Outline each Plasmodium falciparum-infected red blood cell.
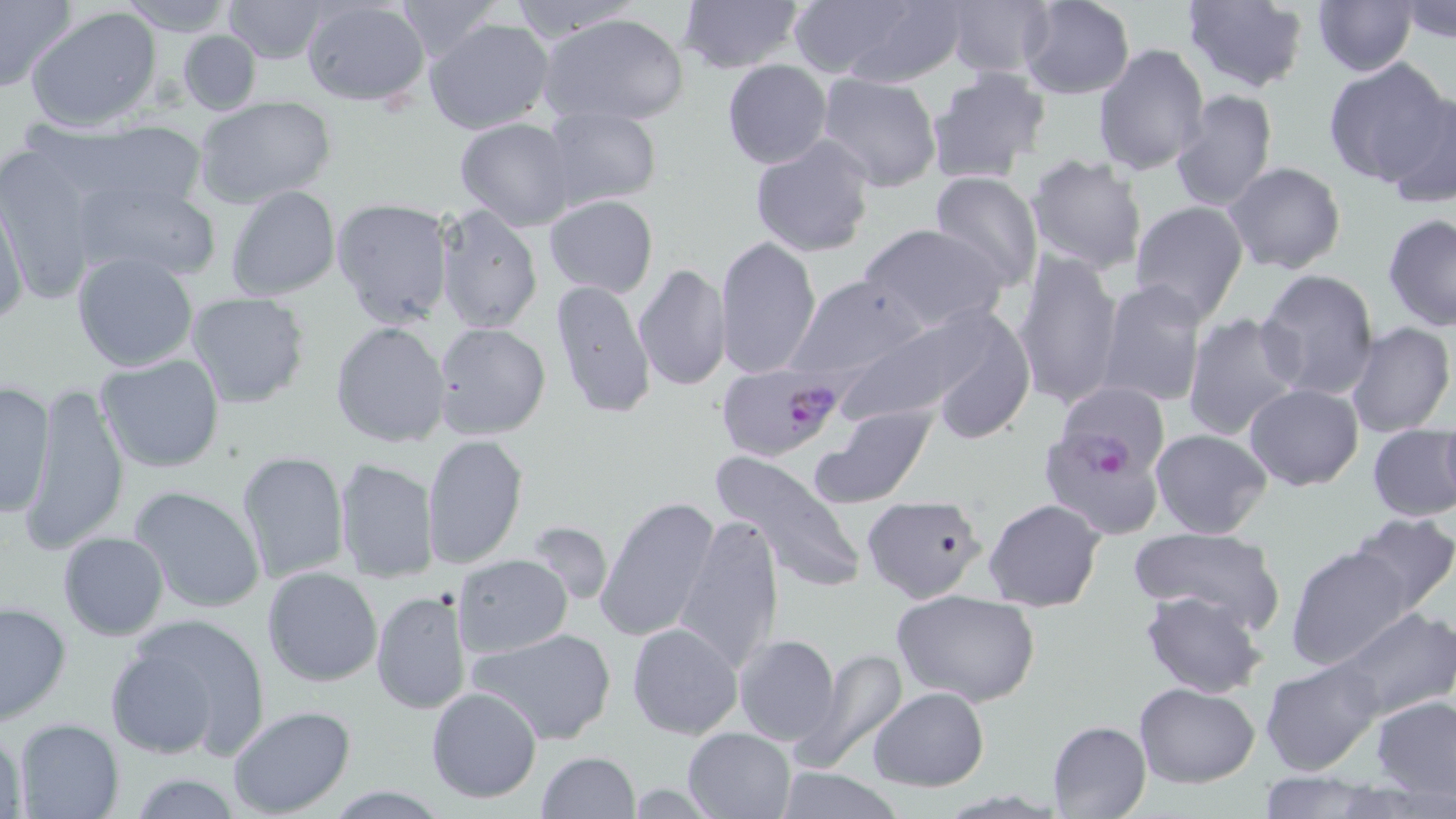

Approximate bounding boxes as (x1, y1, x2, y2) in pixels.
Plasmodium falciparum-infected red blood cells: (716, 364, 839, 462), (1039, 424, 1165, 539).

{
  "slide_level_diagnosis": "Plasmodium falciparum",
  "image_size": "1456×819 pixels",
  "field_of_view": "one of a larger specimen",
  "preparation": "thin blood film",
  "modality": "optical microscopy",
  "uninfected_red_blood_cell_locations": "approximate bounding boxes as (x1, y1, x2, y2) in pixels: (0, 0, 77, 98), (119, 0, 236, 32), (220, 0, 332, 63), (392, 0, 505, 64), (504, 0, 638, 47), (677, 0, 804, 75), (941, 0, 1057, 80), (1016, 0, 1135, 100), (1179, 0, 1310, 93), (1311, 0, 1418, 77), (1398, 0, 1456, 44), (300, 1, 432, 108), (784, 1, 966, 86), (25, 6, 163, 130), (538, 11, 690, 127), (424, 17, 557, 136), (177, 31, 262, 115), (1093, 42, 1211, 176), (1325, 58, 1454, 187), (722, 59, 832, 169), (927, 68, 1055, 186), (816, 72, 944, 194), (1169, 89, 1279, 213), (1382, 91, 1456, 206), (192, 94, 339, 208), (539, 105, 661, 211), (454, 117, 577, 231), (69, 123, 213, 227), (748, 133, 877, 259), (0, 146, 104, 306), (1024, 154, 1149, 274), (1223, 160, 1348, 274), (928, 170, 1045, 292), (73, 171, 221, 285), (226, 185, 342, 300), (1, 193, 30, 328), (544, 194, 658, 298), (330, 198, 454, 330), (1129, 200, 1249, 323), (435, 205, 543, 333), (1382, 213, 1456, 332), (859, 222, 1007, 333), (715, 234, 821, 380), (1011, 248, 1122, 410), (71, 251, 198, 373), (631, 263, 732, 393), (1255, 267, 1382, 399), (790, 274, 926, 383), (1098, 278, 1209, 408), (550, 280, 658, 419), (186, 290, 310, 408), (909, 302, 1035, 445), (1180, 312, 1305, 443), (331, 321, 450, 449), (432, 321, 551, 439), (825, 321, 977, 430), (1343, 322, 1453, 438), (95, 352, 226, 473), (0, 381, 55, 521), (17, 382, 132, 553), (1244, 383, 1363, 491), (815, 405, 937, 507), (1438, 413, 1456, 515), (1367, 424, 1455, 522), (1149, 429, 1273, 540), (421, 433, 529, 570), (712, 450, 866, 592), (235, 451, 349, 584), (335, 457, 437, 584), (129, 485, 268, 616), (595, 493, 721, 642), (862, 495, 987, 603), (983, 498, 1105, 612), (678, 512, 787, 669), (1348, 513, 1456, 616), (523, 521, 613, 608), (1131, 525, 1284, 638), (58, 531, 169, 642), (1284, 542, 1416, 672), (451, 554, 573, 658), (261, 565, 383, 686), (891, 588, 1043, 708), (371, 589, 472, 715), (1140, 589, 1267, 697), (0, 598, 73, 725), (1333, 607, 1455, 719), (109, 617, 268, 761), (627, 621, 743, 738), (470, 625, 618, 746), (733, 634, 841, 746), (795, 648, 908, 771), (1260, 658, 1383, 775), (1134, 682, 1260, 786), (425, 685, 542, 803), (868, 686, 989, 791), (1371, 694, 1456, 799), (226, 705, 356, 818), (2, 715, 29, 818), (11, 717, 124, 819), (1048, 719, 1152, 819), (682, 726, 798, 818), (536, 752, 641, 819), (774, 765, 902, 819), (1254, 771, 1391, 818), (124, 773, 247, 817), (322, 785, 452, 817)",
  "magnification": "1000x",
  "stain": "May-Grünwald-Giemsa"
}